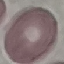

Summary:
  - Malaria status: uninfected
  - Image type: automatically extracted cell patch, resized to 64 × 64 pixels
  - Capture: smartphone camera at the microscope eyepiece
  - Stain: Giemsa
  - Preparation: thin blood smear